Name the blood parasite species.
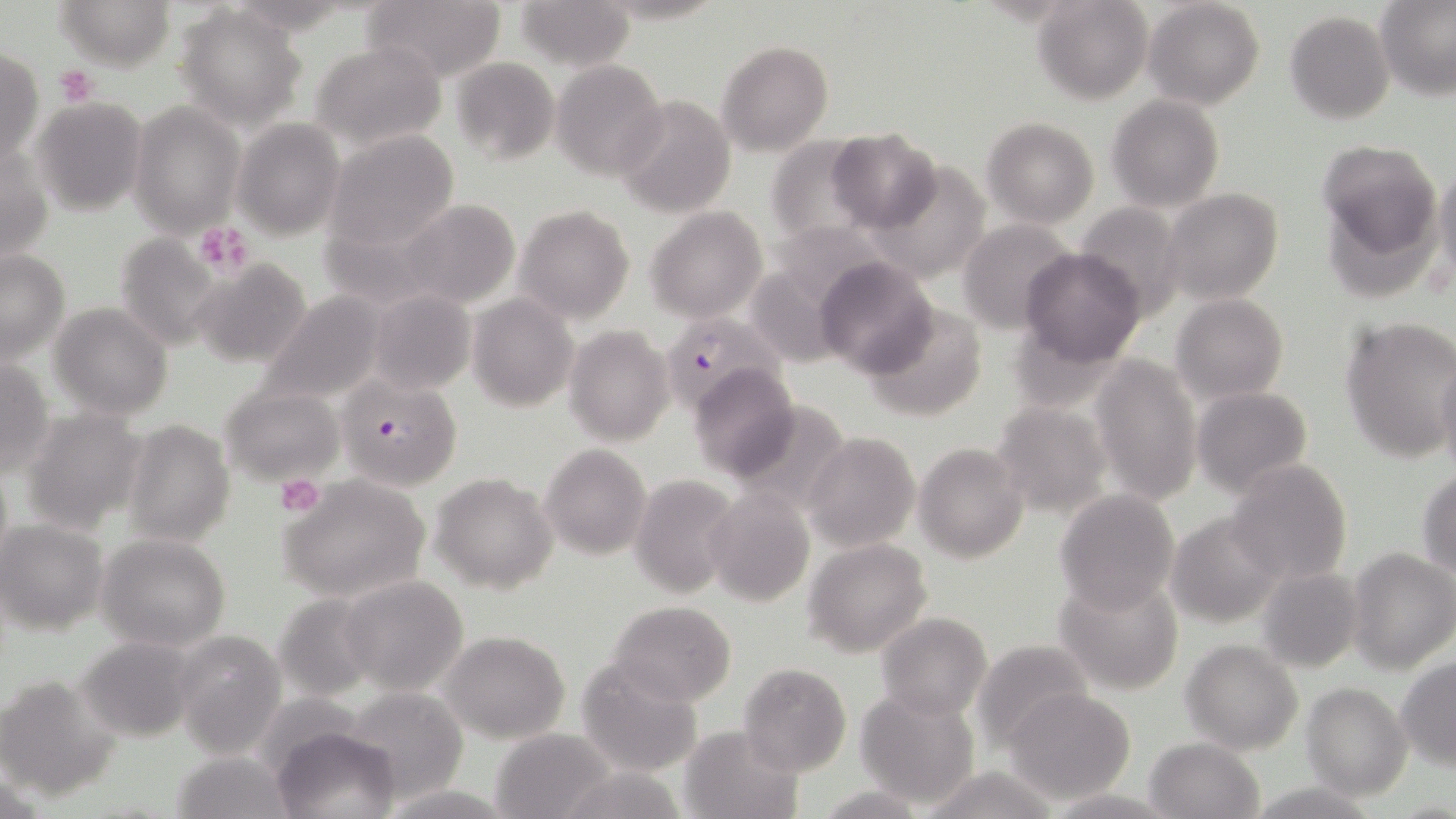

Plasmodium falciparum.

Summary:
  - Coordinate format: approximate bounding boxes as (x1,y1)-(x2,y2) corner pairs in pixels
  - Platelet locations: (55,65)-(99,106), (194,222)-(254,275), (275,474)-(325,516)
  - Uninfected red blood cell locations: (56,0)-(175,70), (360,0)-(507,83), (516,0)-(634,71), (1033,0)-(1152,104), (1143,0)-(1265,111), (1377,2)-(1456,99), (176,4)-(307,127), (1285,10)-(1395,125), (311,40)-(447,151), (716,40)-(833,154), (0,47)-(45,168), (449,57)-(559,164), (552,60)-(669,181), (613,94)-(736,217), (1108,95)-(1226,211), (27,97)-(148,214), (130,101)-(246,238), (231,118)-(346,240), (983,118)-(1099,227), (829,129)-(940,234), (326,130)-(460,251), (764,136)-(878,249), (1318,142)-(1438,258), (1,143)-(52,271), (865,160)-(994,282), (1434,164)-(1456,290), (1160,187)-(1283,304), (395,199)-(522,309), (514,203)-(635,323), (646,207)-(766,321), (959,219)-(1080,334), (112,231)-(228,349), (1019,249)-(1145,367), (0,250)-(72,365), (814,257)-(939,379), (189,259)-(311,367), (368,289)-(477,395), (257,292)-(388,407), (468,293)-(577,411), (1172,293)-(1288,401), (863,301)-(988,423), (50,302)-(173,420), (1340,314)-(1456,462), (565,325)-(674,446), (1434,350)-(1456,473), (1089,353)-(1201,506), (0,359)-(53,479), (689,364)-(798,481), (220,385)-(343,485), (1191,386)-(1313,497), (990,400)-(1111,517), (725,401)-(852,517), (21,408)-(148,533), (121,418)-(235,546), (804,433)-(918,549), (916,443)-(1029,564), (539,444)-(651,562), (1225,459)-(1353,584), (1417,470)-(1456,576), (431,471)-(558,594), (629,474)-(740,598), (277,476)-(429,602), (704,489)-(815,607), (1055,489)-(1180,613), (1164,512)-(1286,625), (1,520)-(109,635), (96,533)-(231,651), (803,539)-(933,656), (1347,548)-(1455,674), (1256,566)-(1363,674), (340,575)-(469,696), (1054,575)-(1185,694), (272,592)-(382,704), (610,601)-(736,706), (875,612)-(992,721), (172,631)-(286,754), (438,631)-(569,743), (75,634)-(200,743), (969,638)-(1094,751), (1181,638)-(1303,754), (575,657)-(705,778), (1397,657)-(1456,768), (737,663)-(852,778), (0,674)-(120,802), (1301,683)-(1412,799), (341,687)-(469,802), (1004,687)-(1137,804), (856,689)-(977,807), (679,724)-(803,818), (274,727)-(402,819), (489,728)-(615,818), (1144,736)-(1265,819), (172,750)-(294,819), (554,764)-(688,819), (918,764)-(1064,819), (1246,780)-(1380,818), (815,783)-(931,818), (377,784)-(513,817)
  - Plasmodium falciparum-infected red blood cell locations: (659,313)-(781,414), (336,374)-(463,491)
  - Preparation: thin blood smear
  - Modality: light microscopy
  - Image size: 1456×819 pixels
  - Field of view: one of a larger specimen
  - Magnification: 1000x
  - Stain: May-Grünwald-Giemsa